State the preparation type.
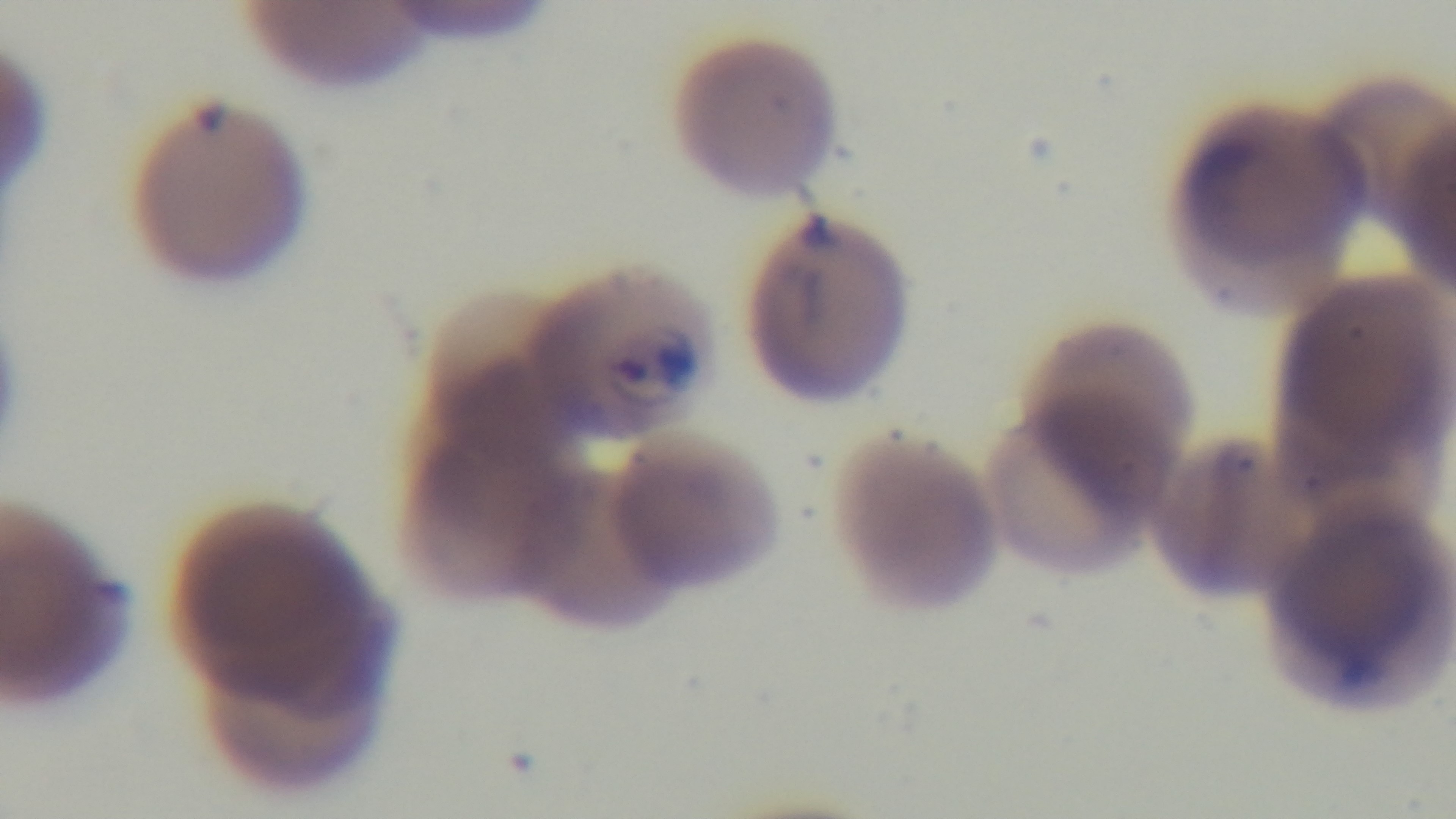

It is a thin blood film.

field of view = one from the slide
malaria status = infected
capture = mounted 4K digital camera
stain = Giemsa
objective = 100x oil immersion
modality = light microscopy